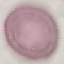

Summary:
  - Result: no malaria parasites seen
  - Preparation: thin blood film
  - Image type: cell patch, automatically extracted from a larger field of view and resized to 64 × 64 pixels
  - Capture: smartphone through the microscope eyepiece
  - Stain: Giemsa